Assess the morphology of the red blood cells.
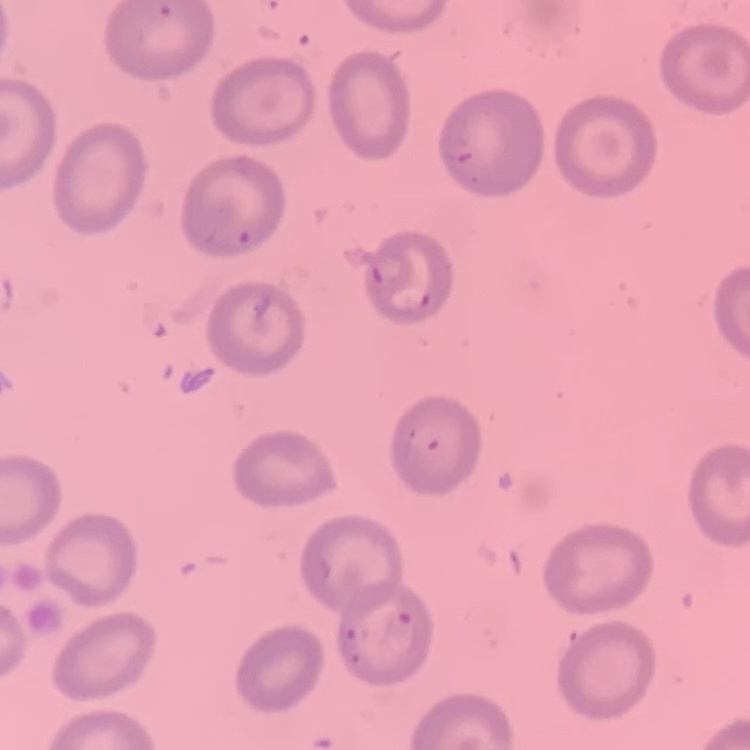
They show no rouleaux formation.

Thin peripheral smear. Square crop of a larger photomicrograph. Stained with either Field's or Giemsa.